Identify the parasite.
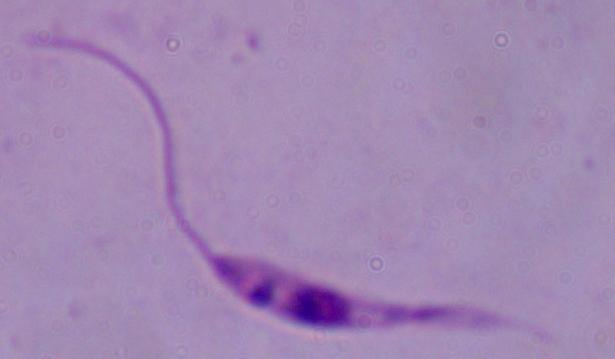

This is Leishmania.

magnification: 1000x
modality: micrograph